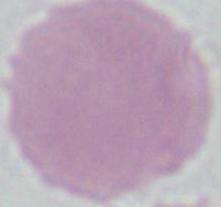

Summary:
  - Magnification: 1000x
  - Modality: photomicrograph
  - Identification: red blood cell